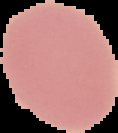

preparation = thin blood smear
image type = segmented cell region on a black background
malaria status = uninfected
image size = 118×133 pixels